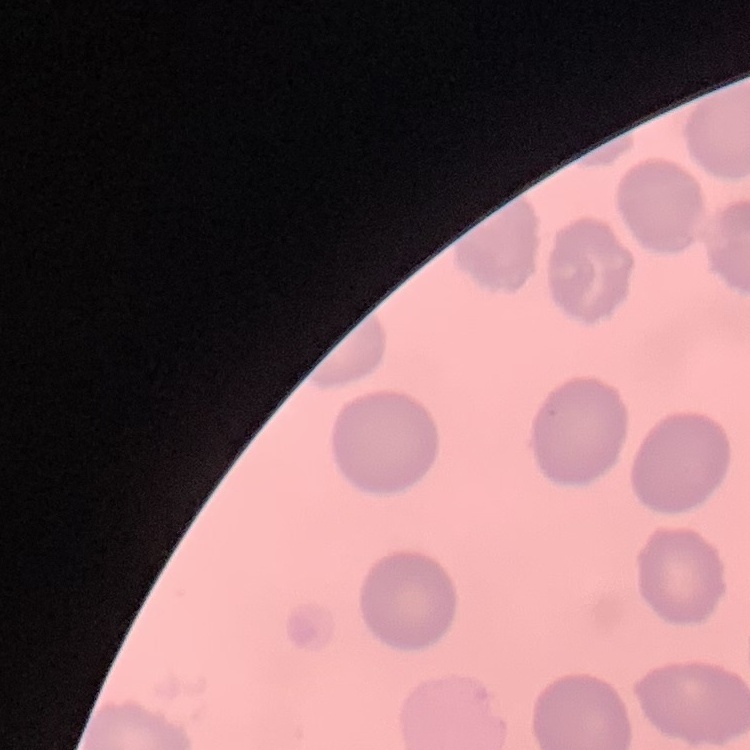
Summary:
  - Red blood cell morphology: no rouleaux formation
  - Image type: square crop of a larger photomicrograph
  - Preparation: thin blood smear
  - Stain: Field's or Giemsa